Give the position of every malaria parasite.
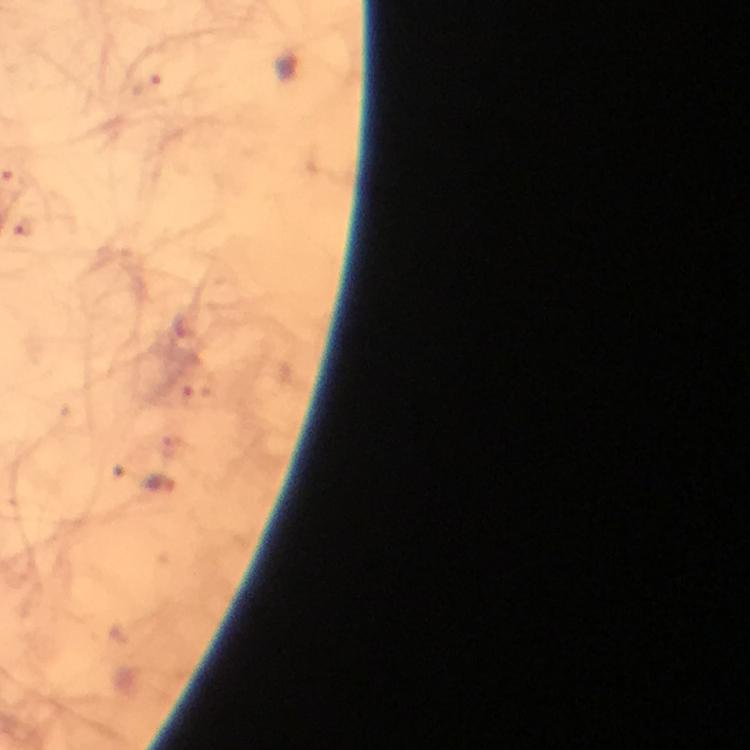

Approximate centers as {x, y} in pixels.
Malaria parasites: {160, 484}.

Summary:
  - Immersion oil: used
  - Preparation: thick blood film
  - Stain: Giemsa
  - Context: from a malaria diagnostic workup
  - Magnification: 100x
  - Image size: 750×750 pixels
  - Cropped from: a single field of view
  - Capture: smartphone camera through the microscope